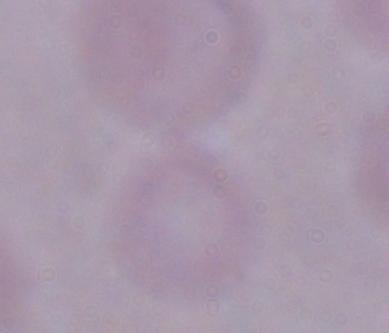
magnification = 1000x
identification = trypanosome
modality = photomicrograph